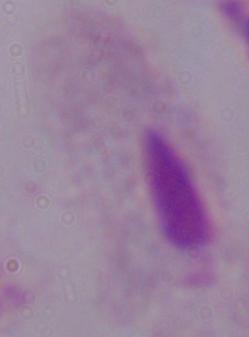
Summary:
  - Modality: photomicrograph
  - Identification: trichomonad
  - Magnification: 1000x